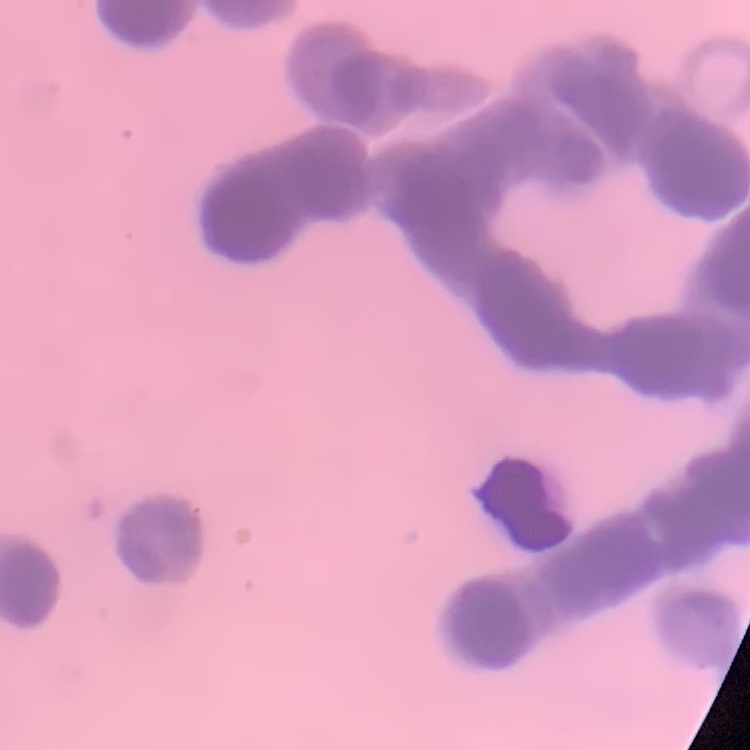
erythrocyte_morphology: rouleaux formation
stain: Field's or Giemsa
image_type: one tile cut from a larger photomicrograph
preparation: thin peripheral smear